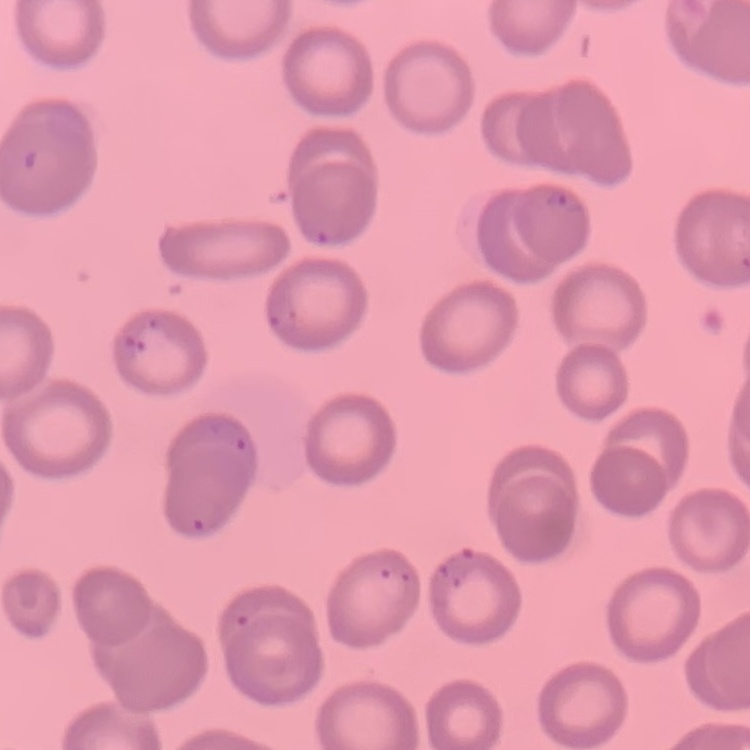

The red blood cells show no rouleaux formation. Thin peripheral smear. Stained with either Field's or Giemsa. Square crop of a larger photomicrograph.